Assess for Plasmodium parasites.
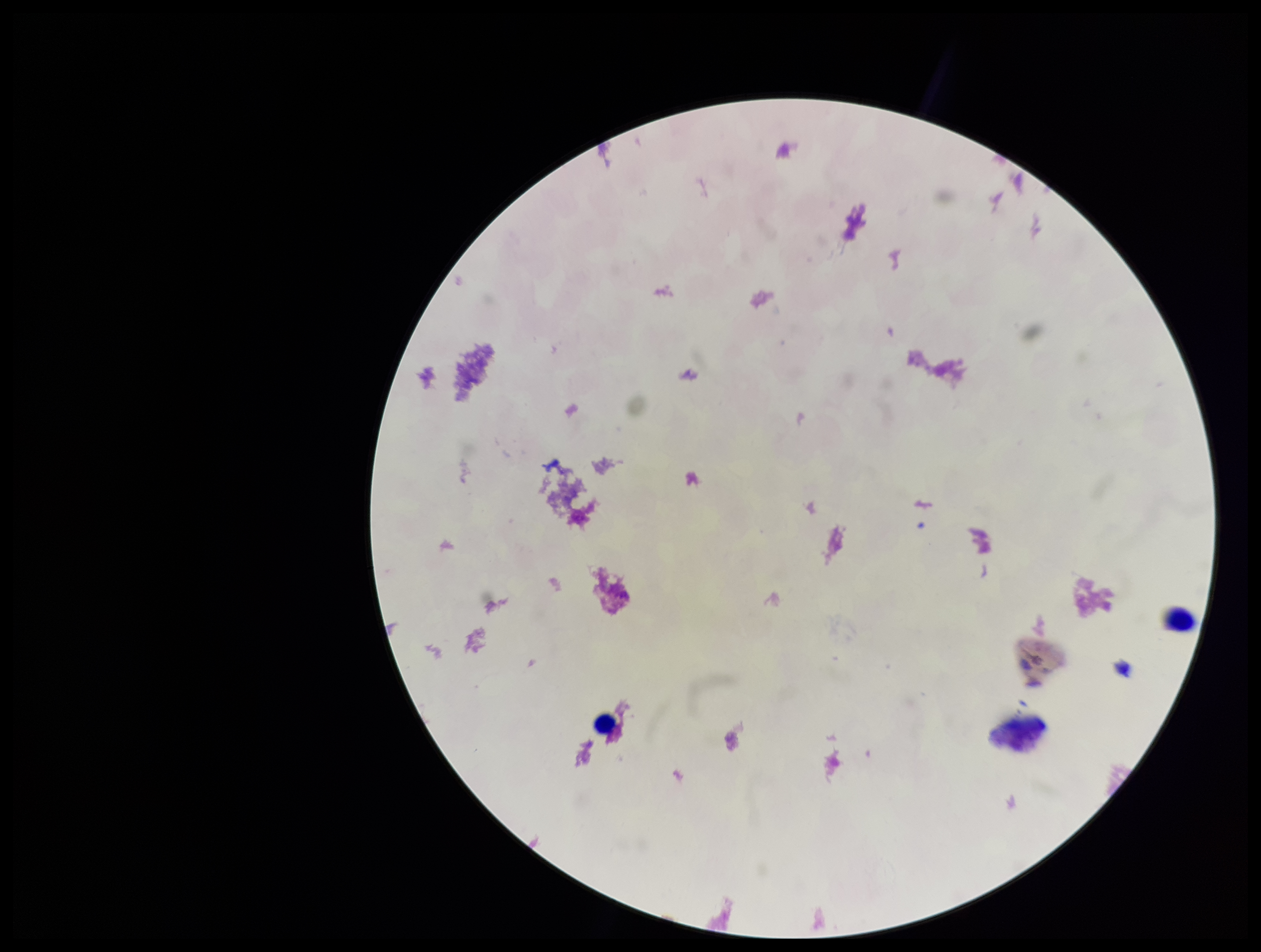
None detected.

One field from this slide. Preparation: thick. Leukocyte count: 2. Giemsa stain. Patient malaria status: negative. Photographed through the microscope eyepiece with a smartphone camera. Parasite count: 0. Image is 1261×952 pixels.